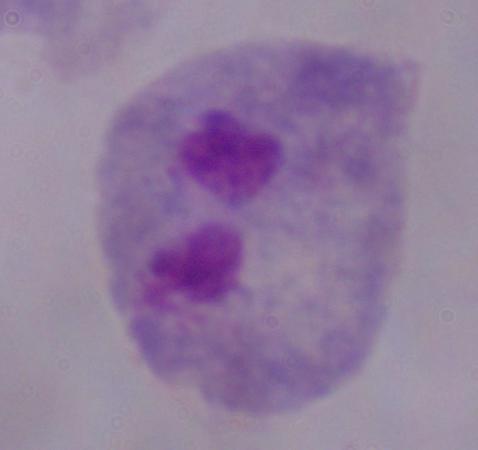
Micrograph. A trichomonad is seen. 1000x magnification.